Describe the morphology of the erythrocytes.
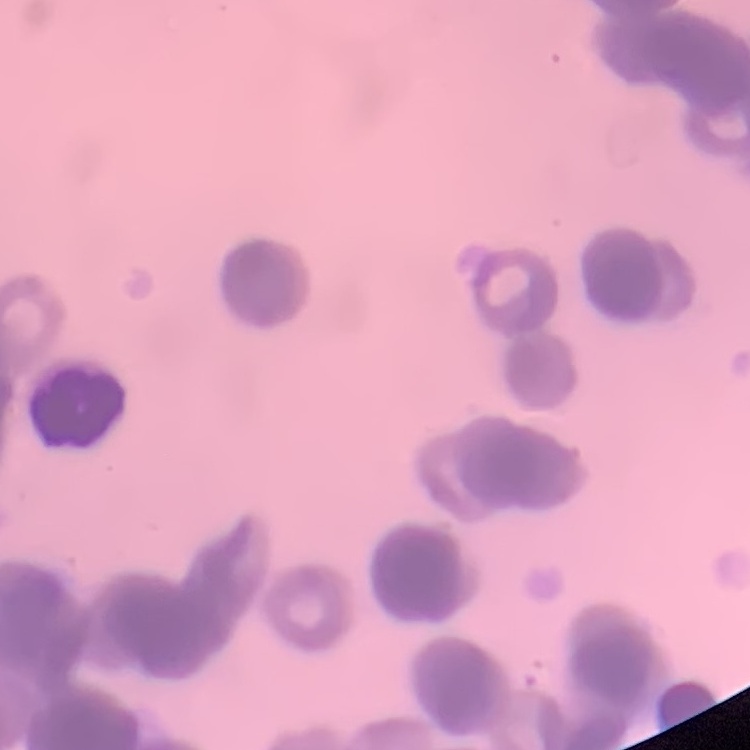

They show rouleaux formation.

Summary:
  - Image type: one tile cut from a larger photomicrograph
  - Stain: Field's or Giemsa
  - Preparation: thin blood smear